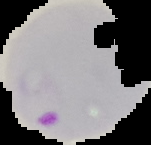

Summary:
  - Image size: 151×145 pixels
  - Preparation: thin blood smear
  - Result: Plasmodium parasites identified
  - Image type: segmented cell region with the area outside set to black